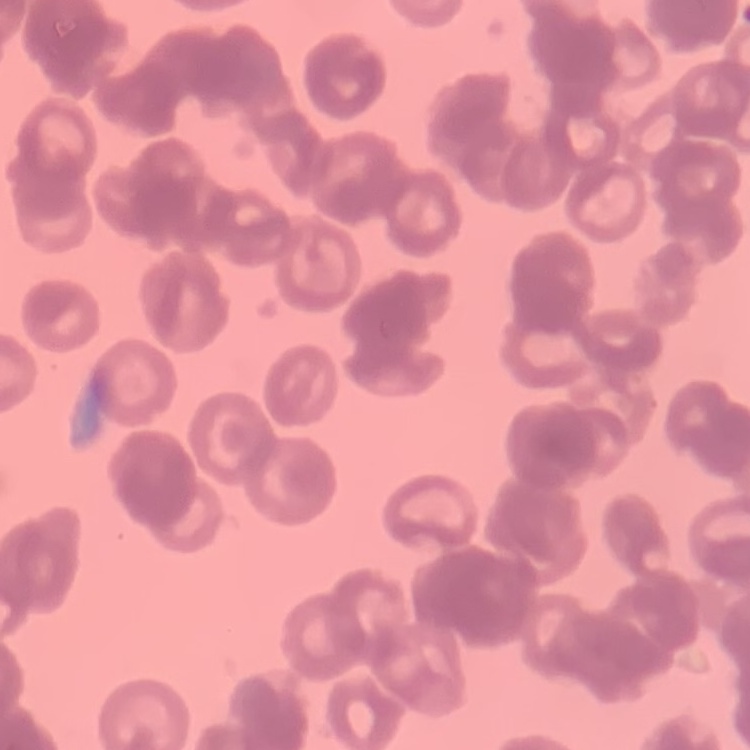
Summary:
  - Red blood cell morphology: rouleaux formation
  - Preparation: thin peripheral smear
  - Image type: one tile cut from a larger photomicrograph
  - Stain: Field's or Giemsa